Give the extent of all Plasmodium falciparum-infected red blood cells.
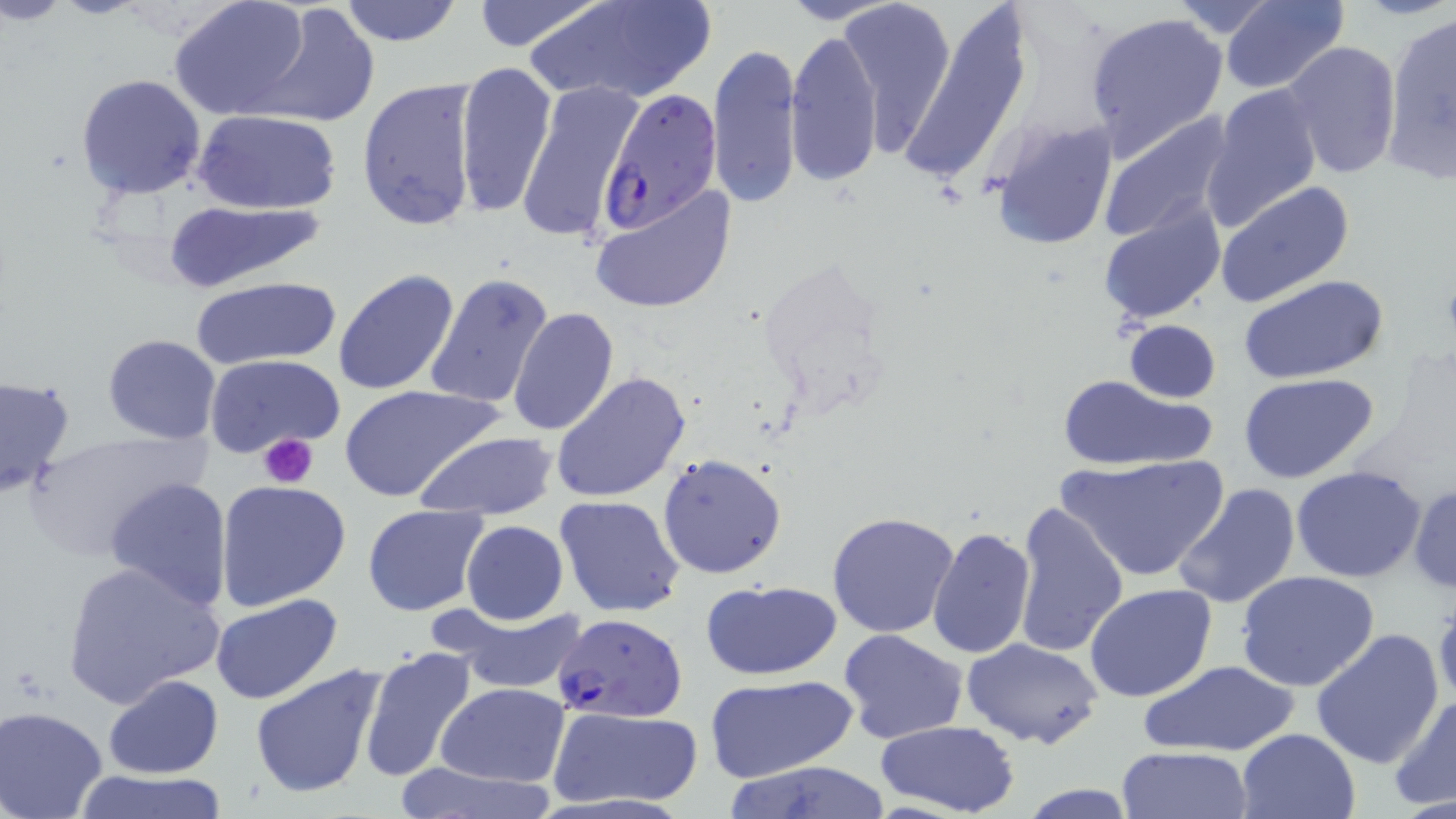
Approximate bounding boxes as named x1/y1/x2/y2 corners in pixels.
Plasmodium falciparum-infected red blood cells: (x1=600, y1=87, x2=724, y2=233), (x1=554, y1=612, x2=687, y2=723).

{
  "slide_level_diagnosis": "Plasmodium falciparum",
  "image_size": "1456×819 pixels",
  "uninfected_red_blood_cell_locations": "approximate bounding boxes as named x1/y1/x2/y2 corners in pixels: (x1=336, y1=0, x2=464, y2=46), (x1=467, y1=0, x2=607, y2=51), (x1=528, y1=0, x2=717, y2=107), (x1=775, y1=0, x2=901, y2=25), (x1=838, y1=0, x2=956, y2=158), (x1=168, y1=1, x2=310, y2=121), (x1=893, y1=1, x2=1033, y2=187), (x1=1164, y1=1, x2=1287, y2=37), (x1=1217, y1=1, x2=1348, y2=94), (x1=247, y1=5, x2=380, y2=128), (x1=1083, y1=9, x2=1229, y2=160), (x1=1382, y1=10, x2=1456, y2=179), (x1=784, y1=27, x2=883, y2=190), (x1=707, y1=39, x2=800, y2=213), (x1=1281, y1=41, x2=1401, y2=182), (x1=453, y1=63, x2=557, y2=222), (x1=74, y1=73, x2=208, y2=199), (x1=357, y1=77, x2=480, y2=233), (x1=517, y1=83, x2=639, y2=246), (x1=1204, y1=83, x2=1324, y2=231), (x1=196, y1=109, x2=340, y2=214), (x1=1097, y1=109, x2=1237, y2=242), (x1=987, y1=118, x2=1117, y2=253), (x1=1215, y1=180, x2=1354, y2=309), (x1=588, y1=184, x2=738, y2=316), (x1=165, y1=198, x2=328, y2=291), (x1=1096, y1=198, x2=1226, y2=326), (x1=332, y1=268, x2=459, y2=396), (x1=425, y1=272, x2=555, y2=410), (x1=1240, y1=274, x2=1390, y2=386), (x1=191, y1=276, x2=340, y2=369), (x1=508, y1=308, x2=620, y2=435), (x1=1122, y1=319, x2=1221, y2=402), (x1=104, y1=334, x2=221, y2=444), (x1=203, y1=354, x2=345, y2=459), (x1=551, y1=372, x2=693, y2=505), (x1=1054, y1=372, x2=1219, y2=473), (x1=1239, y1=372, x2=1380, y2=484), (x1=0, y1=375, x2=74, y2=499), (x1=338, y1=383, x2=501, y2=503), (x1=25, y1=427, x2=206, y2=560), (x1=413, y1=431, x2=558, y2=522), (x1=656, y1=452, x2=787, y2=578), (x1=1055, y1=454, x2=1230, y2=585), (x1=1291, y1=465, x2=1427, y2=583), (x1=105, y1=477, x2=233, y2=611), (x1=215, y1=480, x2=352, y2=611), (x1=1408, y1=481, x2=1456, y2=595), (x1=1172, y1=482, x2=1300, y2=610), (x1=554, y1=494, x2=684, y2=617), (x1=1010, y1=501, x2=1127, y2=661), (x1=361, y1=503, x2=490, y2=616), (x1=826, y1=511, x2=960, y2=638), (x1=461, y1=520, x2=567, y2=623), (x1=927, y1=527, x2=1035, y2=658), (x1=61, y1=559, x2=225, y2=710), (x1=1235, y1=569, x2=1382, y2=693), (x1=699, y1=578, x2=844, y2=681), (x1=1084, y1=583, x2=1218, y2=703), (x1=212, y1=594, x2=342, y2=705), (x1=433, y1=599, x2=591, y2=697), (x1=1310, y1=628, x2=1444, y2=770), (x1=838, y1=629, x2=969, y2=745), (x1=962, y1=639, x2=1106, y2=749), (x1=358, y1=645, x2=479, y2=782), (x1=1144, y1=661, x2=1299, y2=757), (x1=247, y1=663, x2=390, y2=800), (x1=103, y1=675, x2=223, y2=779), (x1=706, y1=675, x2=857, y2=785), (x1=435, y1=682, x2=568, y2=786), (x1=1388, y1=692, x2=1456, y2=812), (x1=549, y1=705, x2=703, y2=809), (x1=0, y1=706, x2=111, y2=819), (x1=875, y1=719, x2=1021, y2=816), (x1=1236, y1=728, x2=1360, y2=818), (x1=1118, y1=747, x2=1252, y2=819), (x1=722, y1=759, x2=894, y2=819), (x1=389, y1=760, x2=560, y2=819), (x1=68, y1=769, x2=229, y2=819), (x1=1013, y1=784, x2=1144, y2=818)",
  "field_of_view": "one of a larger specimen",
  "magnification": "1000x",
  "preparation": "thin blood smear",
  "platelet_locations": "approximate bounding boxes as named x1/y1/x2/y2 corners in pixels: (x1=257, y1=433, x2=320, y2=487)",
  "modality": "optical microscopy",
  "stain": "May-Grünwald-Giemsa"
}